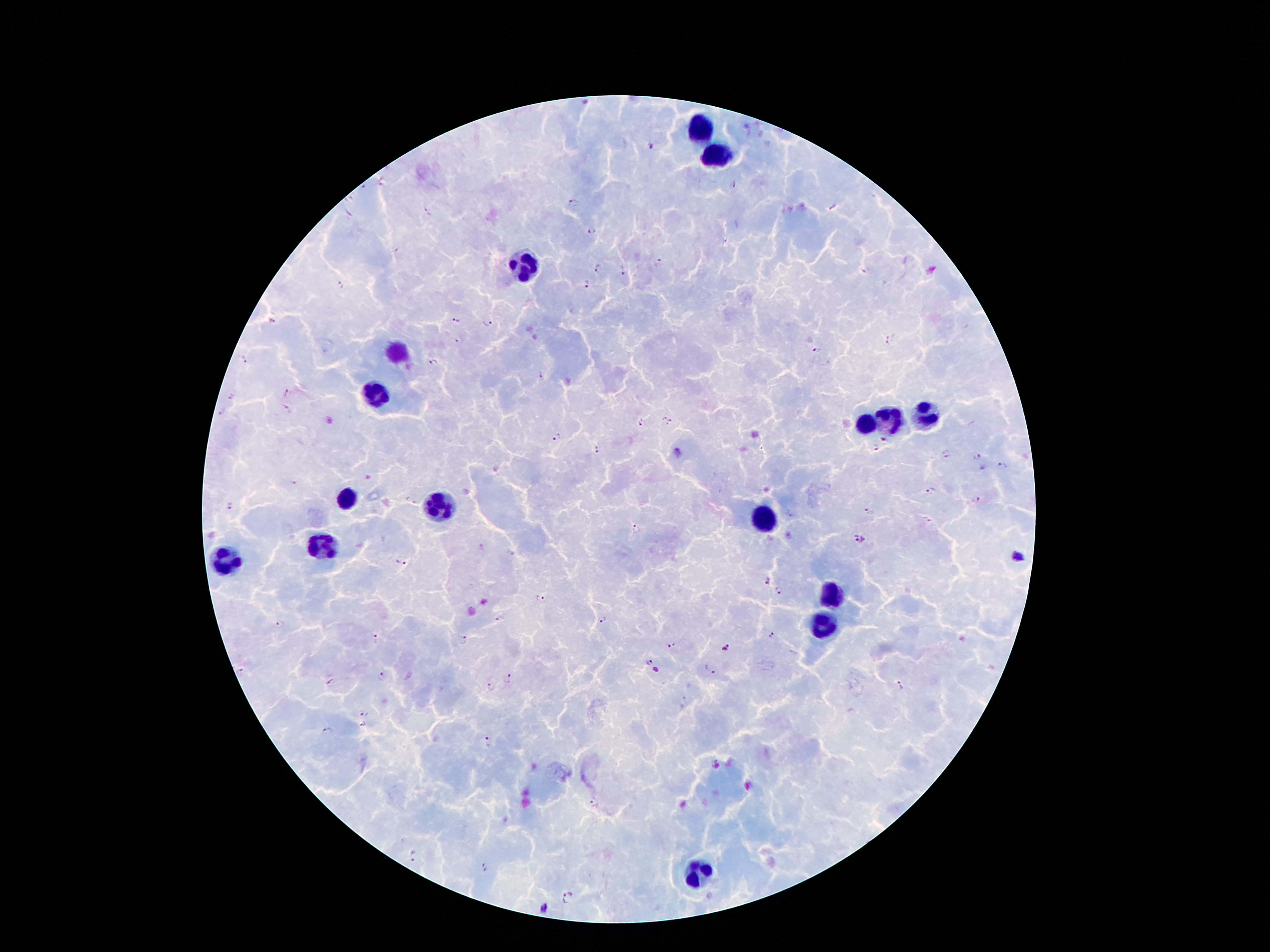

coordinate format = approximate centers as [x, y] in pixels
leukocyte locations = [700, 129], [721, 155], [526, 262], [395, 352], [377, 394], [925, 417], [889, 423], [864, 425], [347, 499], [435, 507], [763, 518], [326, 543], [230, 562], [830, 595], [824, 620], [698, 872]
malaria parasite locations = [653, 146], [731, 183], [572, 203], [833, 207], [590, 230], [395, 250], [598, 269], [622, 271], [865, 271], [588, 283], [341, 284], [455, 317], [271, 320], [487, 322], [889, 340], [460, 341], [816, 349], [243, 360], [436, 364], [538, 376], [288, 392], [233, 397], [284, 408], [221, 414], [667, 420], [642, 422], [557, 438], [876, 448], [596, 450], [946, 454], [975, 458], [1003, 466], [984, 469], [930, 491], [976, 499], [410, 501], [230, 507], [868, 511], [791, 514], [636, 529], [861, 540], [402, 563], [768, 584], [778, 589], [539, 599], [498, 619], [602, 620], [279, 624], [771, 636], [377, 639], [463, 641], [671, 645], [726, 647], [650, 662], [711, 671], [381, 676], [510, 678], [330, 682], [903, 685], [492, 689], [366, 713], [364, 723], [327, 731], [486, 741], [595, 803], [414, 857], [485, 868], [568, 898], [546, 908]
preparation = thick blood film
field of view = single
patient malaria status = infected with Plasmodium falciparum
image size = 1270×952 pixels
magnification = 100x
capture = smartphone camera through the microscope eyepiece
stain = Giemsa